Identify the parasite.
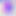
This is Toxoplasma gondii.

magnification = 400x
modality = micrograph